Classify this cell by malaria status.
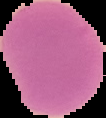
It is uninfected.

Summary:
  - Preparation: thin blood smear
  - Image size: 106×118 pixels
  - Image type: segmented cell region on a black background